Locate and identify every blood parasite.
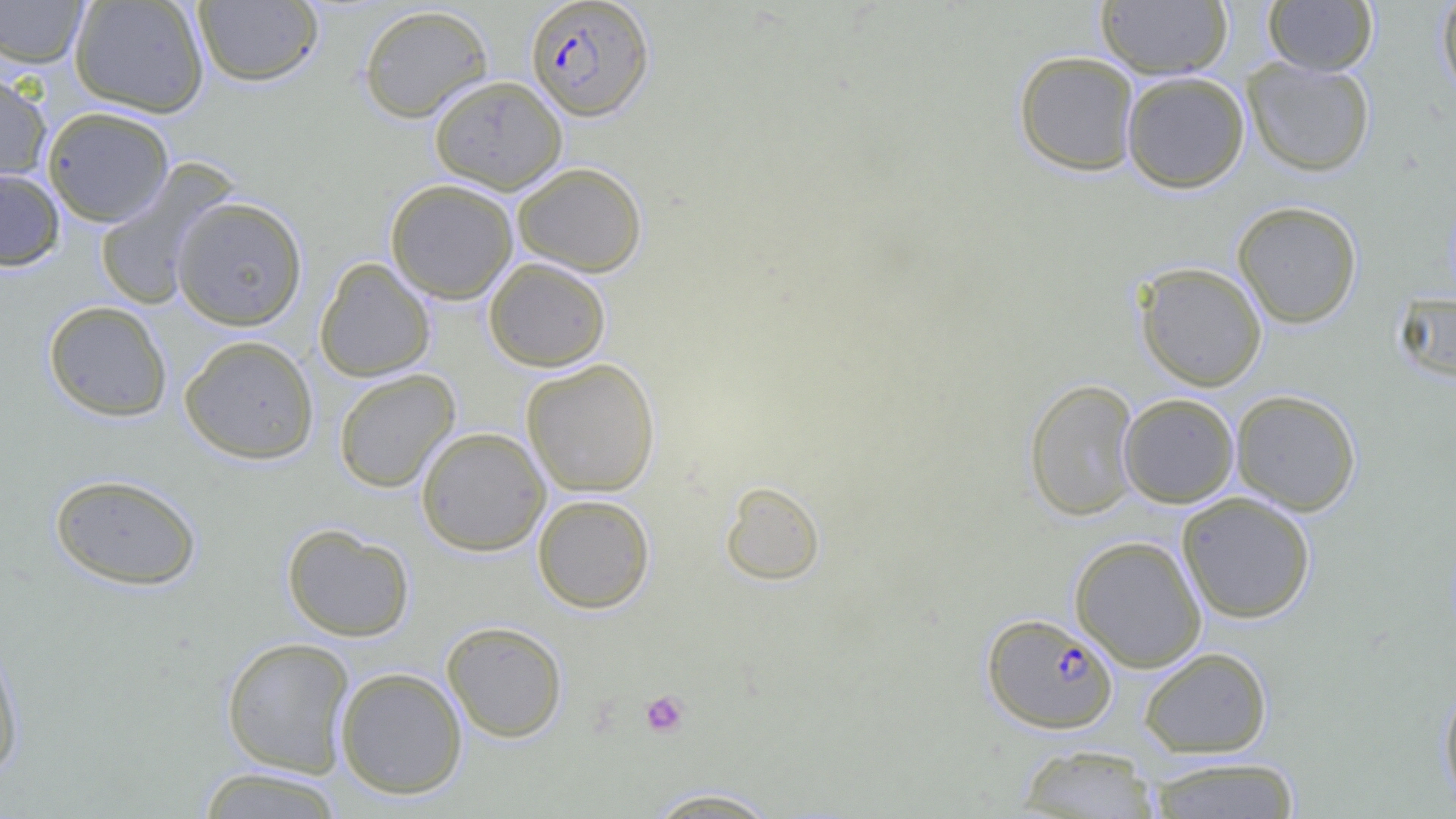

Approximate bounding boxes as named x1/y1/x2/y2 corners in pixels.
Plasmodium falciparum-infected red blood cells: (x1=525, y1=0, x2=655, y2=120), (x1=981, y1=613, x2=1119, y2=733).
No Plasmodium ovale, Plasmodium malariae, Plasmodium vivax, Babesia divergens, or Trypanosoma brucei observed.

Summary:
  - Platelet locations: (x1=639, y1=690, x2=690, y2=738)
  - Uninfected red blood cell locations: (x1=69, y1=0, x2=210, y2=117), (x1=1095, y1=0, x2=1232, y2=79), (x1=1263, y1=0, x2=1377, y2=76), (x1=1435, y1=0, x2=1456, y2=103), (x1=0, y1=1, x2=90, y2=67), (x1=193, y1=1, x2=323, y2=87), (x1=358, y1=3, x2=494, y2=123), (x1=1013, y1=50, x2=1140, y2=176), (x1=1242, y1=57, x2=1376, y2=177), (x1=0, y1=68, x2=52, y2=185), (x1=1121, y1=71, x2=1250, y2=193), (x1=429, y1=75, x2=567, y2=194), (x1=42, y1=106, x2=174, y2=227), (x1=93, y1=159, x2=238, y2=310), (x1=512, y1=161, x2=648, y2=277), (x1=0, y1=167, x2=65, y2=272), (x1=385, y1=179, x2=518, y2=304), (x1=171, y1=195, x2=308, y2=331), (x1=1232, y1=200, x2=1363, y2=329), (x1=314, y1=257, x2=435, y2=382), (x1=483, y1=257, x2=611, y2=371), (x1=1134, y1=261, x2=1267, y2=391), (x1=1393, y1=292, x2=1456, y2=384), (x1=42, y1=300, x2=173, y2=422), (x1=179, y1=334, x2=319, y2=465), (x1=521, y1=358, x2=661, y2=497), (x1=334, y1=369, x2=460, y2=492), (x1=1024, y1=378, x2=1140, y2=521), (x1=1230, y1=389, x2=1361, y2=515), (x1=1118, y1=393, x2=1239, y2=508), (x1=415, y1=426, x2=550, y2=555), (x1=49, y1=472, x2=202, y2=591), (x1=720, y1=480, x2=825, y2=585), (x1=1177, y1=492, x2=1316, y2=624), (x1=532, y1=493, x2=655, y2=613), (x1=281, y1=523, x2=415, y2=642), (x1=1069, y1=534, x2=1207, y2=671), (x1=442, y1=620, x2=568, y2=743), (x1=0, y1=633, x2=26, y2=781), (x1=221, y1=637, x2=355, y2=776), (x1=1139, y1=647, x2=1273, y2=759), (x1=335, y1=666, x2=468, y2=799), (x1=1438, y1=676, x2=1456, y2=811), (x1=1015, y1=744, x2=1160, y2=818), (x1=1142, y1=756, x2=1303, y2=818), (x1=195, y1=766, x2=348, y2=818), (x1=641, y1=786, x2=784, y2=818)
  - Slide-level diagnosis: Plasmodium falciparum
  - Field of view: single
  - Magnification: 1000x
  - Preparation: thin blood film
  - Image size: 1456×819 pixels
  - Modality: optical microscopy